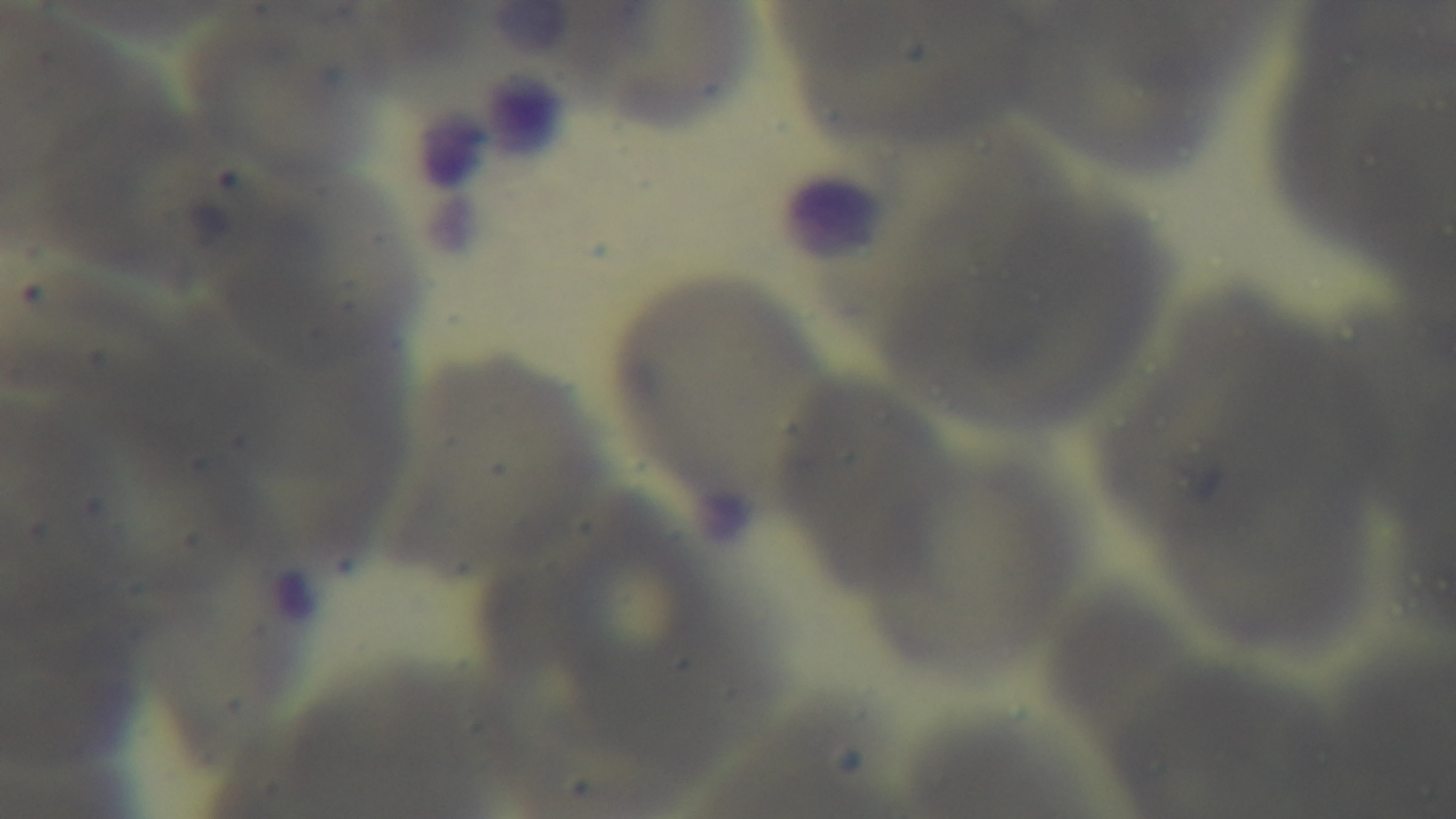
objective = 100x oil immersion
modality = light microscopy
capture = mounted 4K digital camera
field of view = single
preparation = thin blood film
malaria status = uninfected
stain = Giemsa